Identify the parasite.
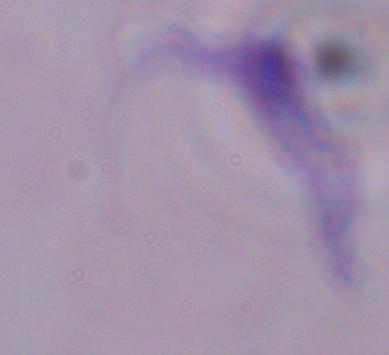
A trypanosome.

Summary:
  - Magnification: 1000x
  - Modality: photomicrograph